State which parasite is depicted.
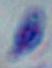
This is Toxoplasma gondii.

Photomicrograph. 1000x magnification.